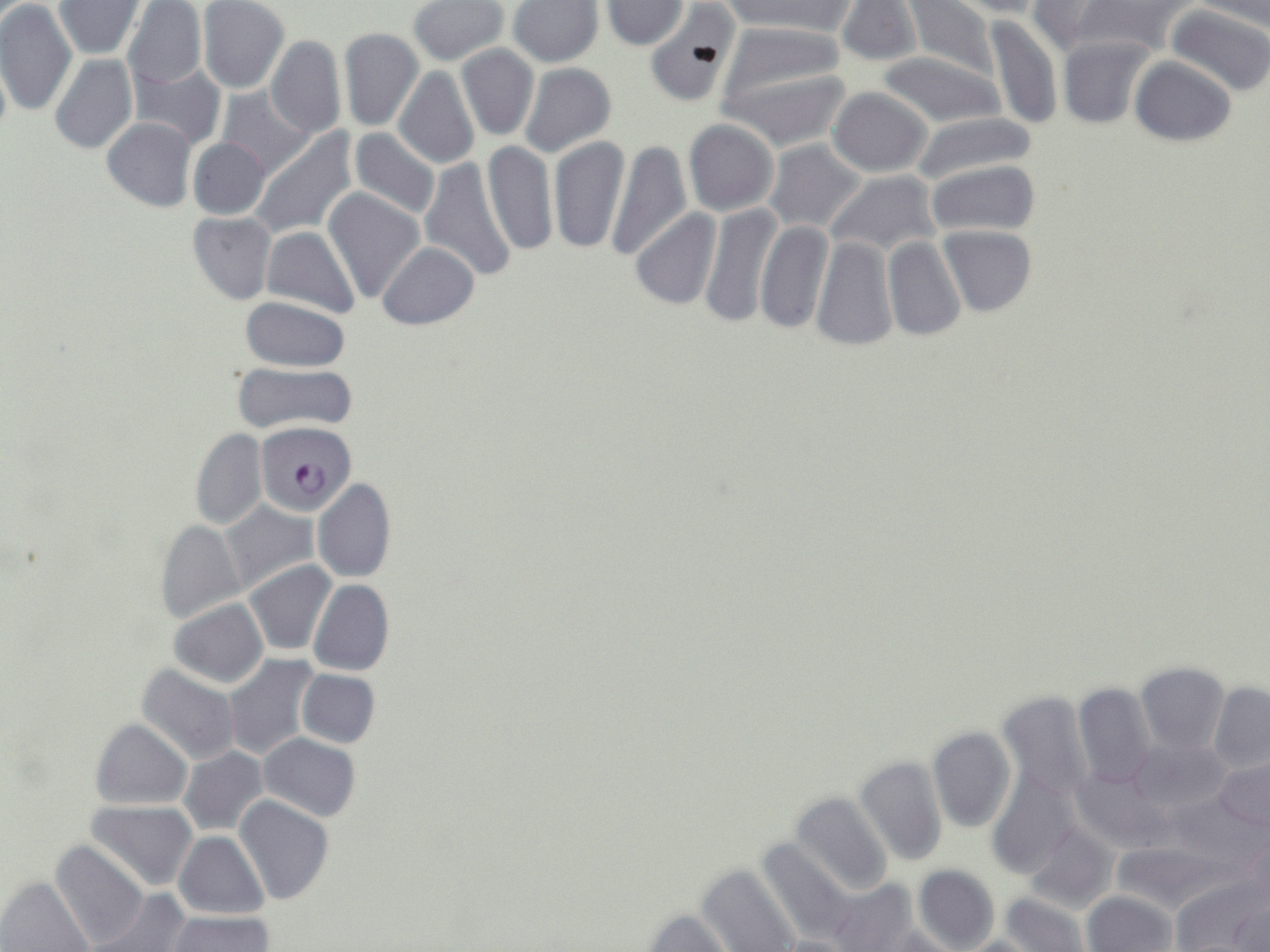
{
  "slide_level_diagnosis": "Plasmodium falciparum",
  "field_of_view": "one of a larger specimen",
  "preparation": "thin blood smear",
  "magnification": "1000x",
  "image_size": "1270×952 pixels",
  "stain": "May-Grünwald-Giemsa",
  "uninfected_red_blood_cell_locations": "approximate bounding boxes as [x1, y1, x2, y2] in pixels: [409, 0, 509, 65], [507, 0, 604, 67], [717, 0, 858, 35], [905, 0, 998, 81], [950, 0, 1051, 17], [0, 1, 77, 118], [53, 1, 145, 58], [122, 1, 207, 89], [198, 1, 289, 93], [835, 1, 922, 67], [1027, 1, 1121, 57], [1074, 1, 1199, 57], [600, 2, 687, 50], [1190, 2, 1270, 28], [644, 4, 741, 107], [1166, 4, 1270, 97], [985, 14, 1063, 130], [718, 20, 847, 110], [338, 27, 424, 132], [1057, 35, 1154, 129], [265, 36, 347, 140], [457, 45, 538, 141], [877, 51, 1007, 129], [0, 53, 11, 148], [49, 54, 137, 155], [1129, 56, 1236, 147], [132, 62, 225, 151], [518, 63, 615, 158], [393, 67, 481, 169], [722, 67, 853, 153], [827, 87, 931, 177], [217, 88, 314, 180], [911, 113, 1035, 187], [102, 118, 197, 212], [683, 120, 778, 217], [251, 128, 357, 237], [349, 128, 441, 220], [549, 136, 630, 255], [189, 137, 269, 219], [605, 139, 690, 261], [763, 139, 868, 235], [481, 142, 557, 256], [419, 157, 519, 283], [925, 158, 1040, 237], [824, 171, 939, 260], [323, 187, 425, 305], [699, 202, 782, 328], [630, 209, 721, 311], [188, 211, 276, 304], [755, 218, 833, 333], [262, 226, 360, 320], [939, 226, 1036, 317], [811, 234, 896, 351], [882, 237, 965, 342], [378, 240, 479, 329], [241, 296, 350, 372], [232, 362, 356, 434], [190, 430, 268, 530], [312, 478, 396, 583], [219, 500, 318, 595], [155, 518, 245, 625], [244, 561, 336, 656], [308, 580, 395, 677], [167, 598, 269, 689], [223, 653, 320, 761], [1136, 662, 1230, 754], [136, 664, 242, 767], [295, 669, 380, 749], [1209, 682, 1270, 773], [1073, 683, 1156, 788], [995, 690, 1094, 801], [90, 717, 192, 810], [927, 727, 1016, 834], [259, 733, 361, 822], [1125, 736, 1233, 821], [176, 746, 268, 836], [855, 756, 947, 867], [1214, 756, 1270, 832], [1070, 766, 1170, 854], [988, 770, 1079, 876], [1164, 790, 1264, 874], [789, 791, 893, 896], [233, 795, 334, 906], [88, 800, 199, 893], [1023, 823, 1118, 914], [1241, 829, 1269, 916], [174, 831, 267, 919], [755, 836, 855, 946], [50, 841, 149, 948], [1109, 841, 1225, 914], [697, 863, 800, 952], [913, 864, 999, 952], [1169, 875, 1265, 952], [2, 876, 95, 951], [826, 877, 918, 952], [87, 887, 192, 952], [1084, 890, 1177, 952], [999, 892, 1091, 952], [1231, 894, 1269, 951], [637, 909, 736, 952], [166, 911, 275, 952], [864, 927, 966, 952], [765, 935, 860, 952], [953, 937, 1044, 952]",
  "modality": "optical microscopy",
  "plasmodium_falciparum_infected_red_blood_cell_locations": "approximate bounding boxes as [x1, y1, x2, y2] in pixels: [256, 421, 356, 516]"
}